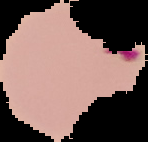
The area outside the segmented cell region is set to black. Result: malaria parasites identified. From a thin blood film. Image is 148×142 pixels.